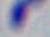 Micrograph. Captured at 1000x magnification. Toxoplasma gondii is shown.